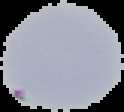

From a thin blood smear. Result: no Plasmodium parasites detected. The area outside the segmented cell region is set to black. Image is 124×112 pixels.